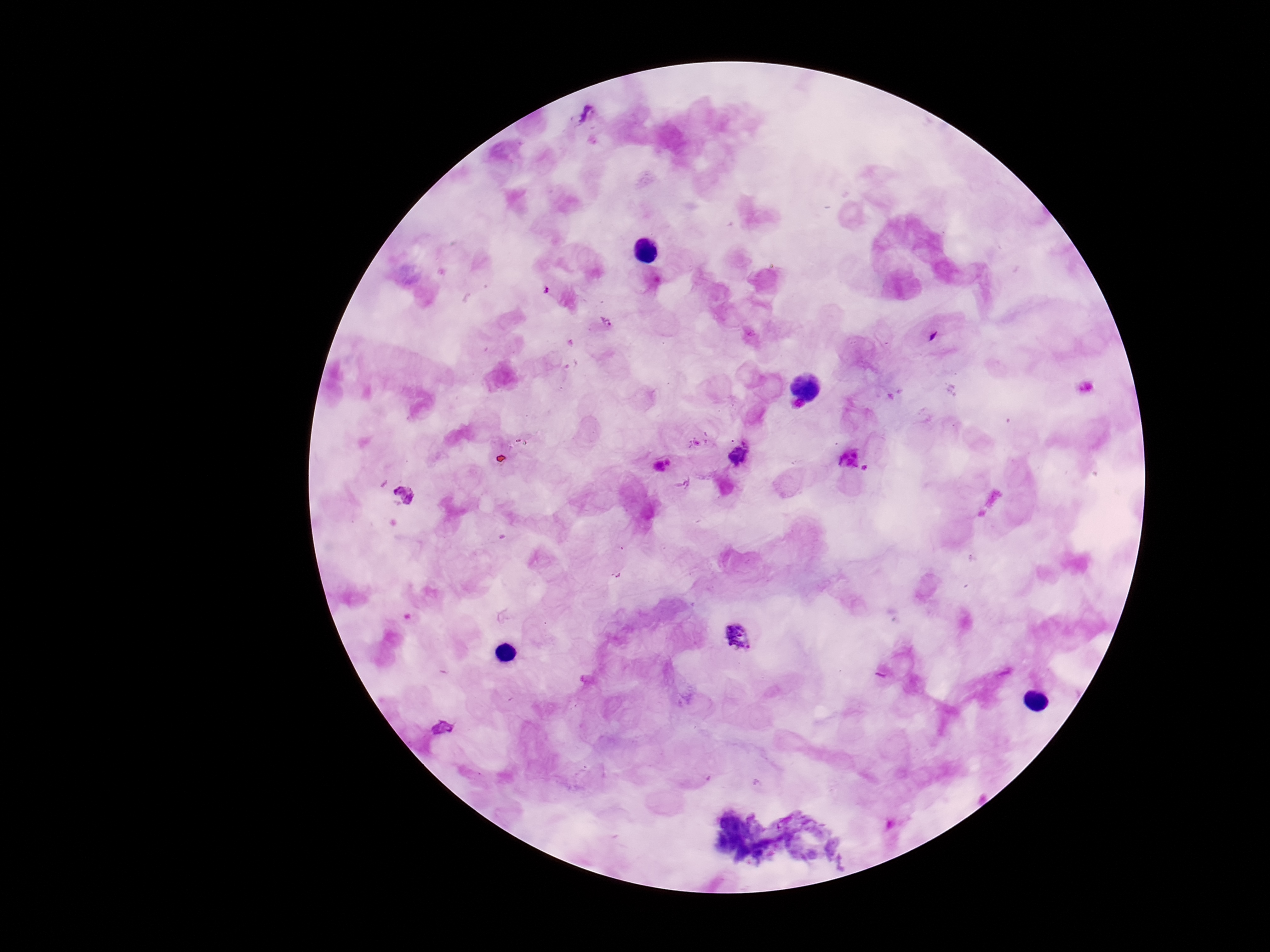
Approximate centers as (x, y) in pixels. Plasmodium parasite locations: (586, 116), (606, 321), (739, 455), (851, 457), (737, 636), (443, 726). Thick blood film. Single field of view. Patient malaria status: positive. Image is 1270×952 pixels. Giemsa-stained preparation. Smartphone photograph taken through the microscope eyepiece. 100x magnification.